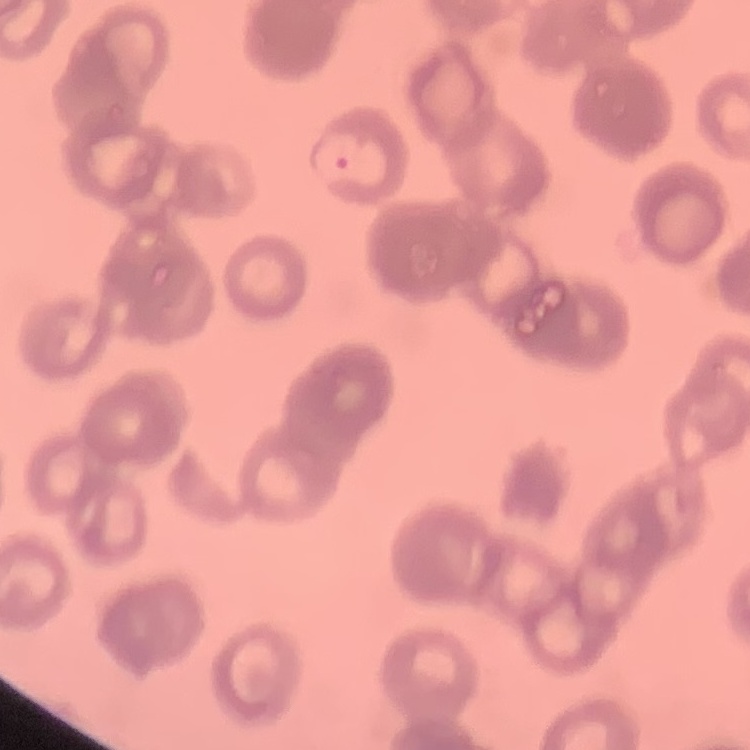
erythrocyte morphology = rouleaux formation
preparation = thin blood smear
stain = Field's or Giemsa
image type = square crop of a larger photomicrograph